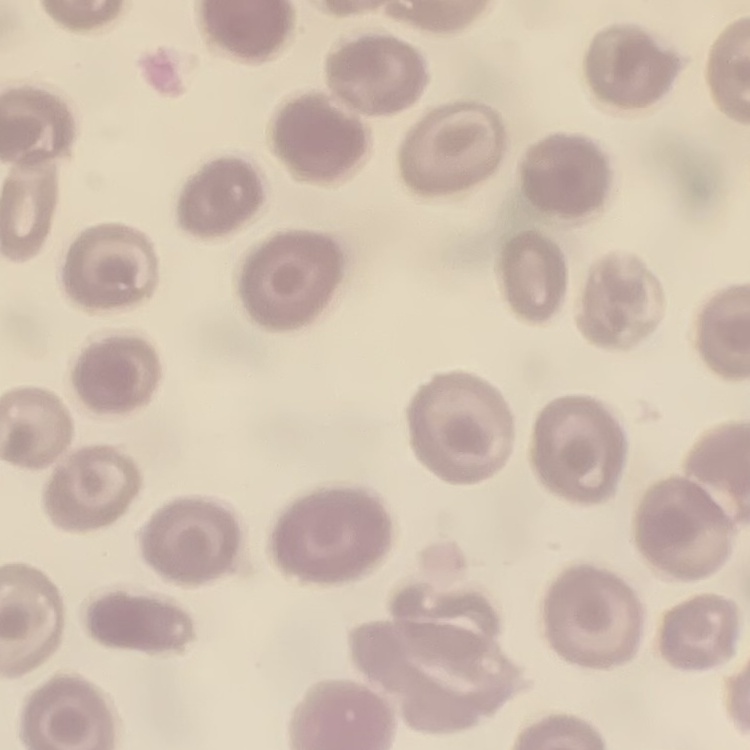
red blood cell morphology = no rouleaux formation
stain = Field's or Giemsa
image type = square crop of a larger photomicrograph
preparation = thin peripheral smear